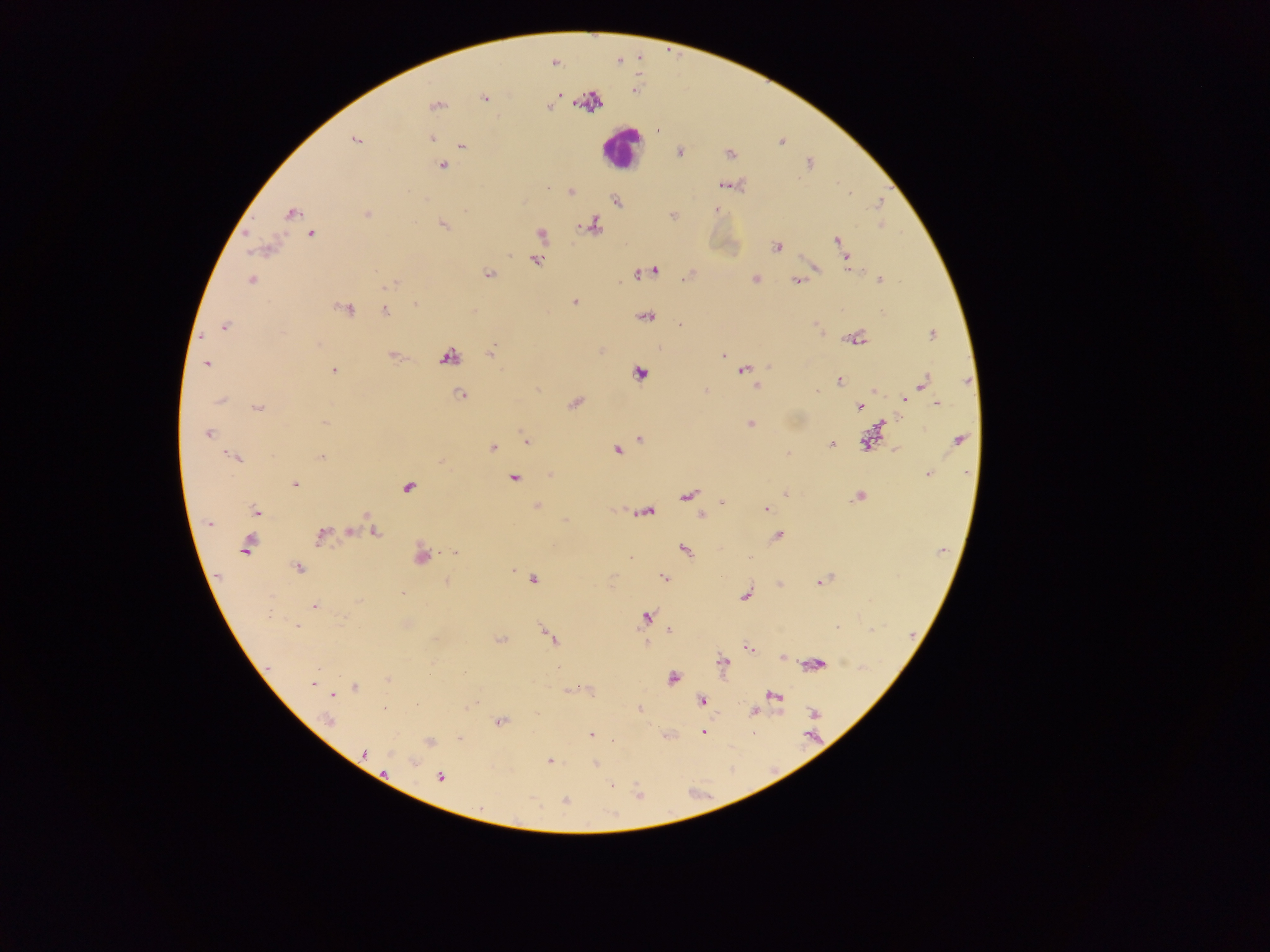
Approximate centers as [x, y] in pixels.
Summary:
  - Plasmodium parasite locations: [554, 63], [560, 95], [485, 98], [436, 105], [550, 107], [431, 138], [355, 140], [462, 146], [679, 152], [810, 163], [442, 166], [724, 184], [571, 192], [849, 192], [616, 201], [880, 203], [716, 209], [292, 213], [367, 214], [443, 224], [880, 225], [594, 226], [312, 234], [541, 234], [837, 239], [776, 246], [847, 260], [536, 261], [848, 267], [814, 268], [376, 271], [653, 271], [488, 274], [639, 274], [687, 276], [755, 279], [880, 280], [251, 281], [796, 281], [390, 285], [573, 302], [415, 304], [347, 310], [840, 310], [882, 310], [385, 311], [647, 317], [815, 323], [224, 326], [932, 335], [857, 339], [490, 353], [449, 356], [724, 356], [206, 364], [769, 367], [744, 370], [334, 371], [640, 373], [839, 381], [923, 382], [757, 386], [706, 390], [816, 390], [874, 390], [460, 394], [221, 400], [905, 400], [574, 403], [937, 403], [258, 407], [859, 407], [325, 422], [750, 423], [880, 425], [208, 434], [639, 438], [959, 440], [526, 442], [865, 442], [831, 444], [493, 447], [617, 449], [787, 453], [235, 458], [321, 458], [927, 474], [513, 479], [295, 483], [409, 487], [785, 493], [688, 495], [858, 497], [722, 502], [536, 507], [765, 508], [256, 511], [648, 512], [701, 515], [209, 524], [350, 532], [375, 532], [321, 535], [778, 536], [247, 545], [684, 549], [455, 553], [422, 556], [298, 568], [664, 577], [534, 580], [822, 581], [447, 582], [402, 593], [745, 596], [357, 601], [314, 606], [646, 617], [296, 625], [837, 627], [669, 631], [551, 638], [500, 640], [645, 643], [748, 649], [782, 657], [723, 663], [817, 664], [672, 678], [389, 679], [313, 684], [355, 687], [774, 696], [702, 701], [417, 705], [384, 708], [638, 710], [752, 712], [813, 713], [329, 721], [500, 721], [704, 732], [591, 735], [460, 738], [429, 742], [365, 753], [549, 761], [413, 762], [596, 764], [385, 772], [441, 778], [611, 786], [565, 800]
  - Leukocyte locations: [620, 148]
  - Country: Ghana
  - Preparation: thick blood film
  - Field of view: single
  - Capture: mobile-phone photograph through a microscope
  - Image size: 1270×952 pixels